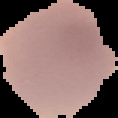

image type = segmented cell region on a black background
image size = 118×118 pixels
malaria status = uninfected
preparation = thin blood smear